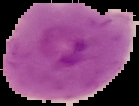
{
  "preparation": "thin blood film",
  "image_size": "139×106 pixels",
  "image_type": "cell region segmented out of the field of view; surrounding area masked to black",
  "result": "malaria parasites detected"
}